State which cell type is depicted.
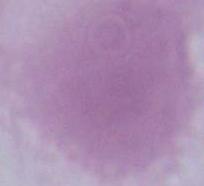

This is an erythrocyte.

Summary:
  - Modality: photomicrograph
  - Magnification: 1000x